Report the malaria status of this cell.
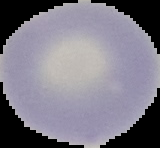
Uninfected.

Summary:
  - Image type: cell region segmented out of the field of view; surrounding area masked to black
  - Image size: 160×148 pixels
  - Preparation: thin blood smear